Classify the preparation.
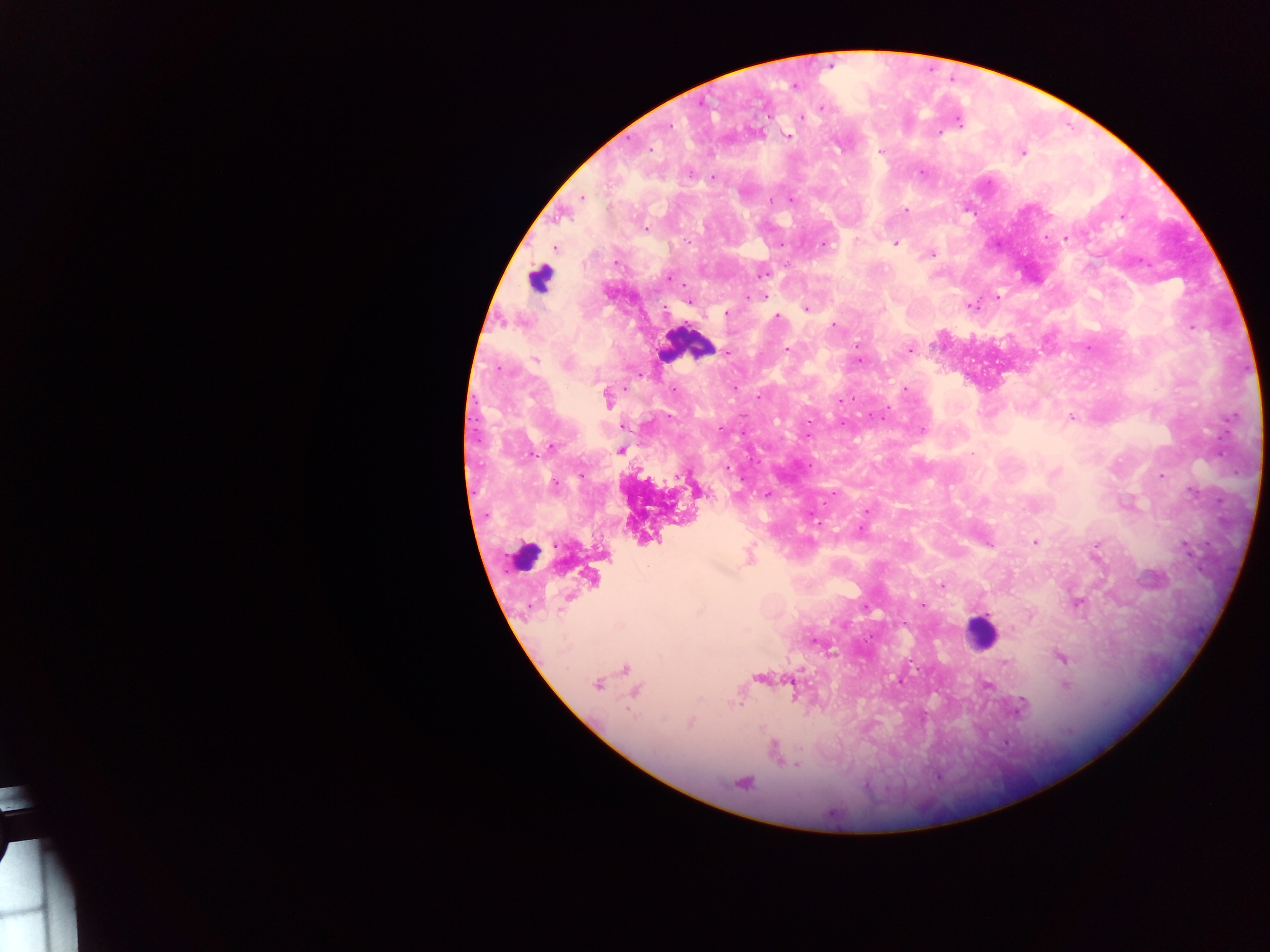
Thick blood film.

Approximate centers as {x, y} in pixels. Leukocyte locations: {540, 277}, {686, 344}, {522, 556}, {980, 631}. Plasmodium parasite locations: {829, 66}, {794, 85}, {823, 107}, {801, 117}, {959, 123}, {668, 125}, {939, 132}, {786, 136}, {649, 149}, {881, 152}, {1021, 152}, {921, 172}, {712, 177}, {582, 197}, {905, 211}, {1122, 217}, {646, 228}, {1066, 238}, {824, 243}, {895, 243}, {553, 247}, {930, 253}, {762, 272}, {671, 278}, {764, 296}, {997, 297}, {688, 300}, {971, 306}, {806, 308}, {726, 313}, {778, 317}, {833, 325}, {1192, 327}, {787, 349}, {909, 349}, {727, 352}, {535, 359}, {858, 360}, {672, 390}, {904, 390}, {606, 397}, {1070, 417}, {624, 425}, {922, 430}, {551, 447}, {620, 450}, {726, 469}, {1162, 476}, {554, 484}, {698, 489}, {766, 494}, {866, 511}, {1035, 542}, {987, 543}, {1095, 550}, {748, 556}, {591, 577}, {941, 585}, {1077, 603}, {923, 605}, {816, 642}, {1061, 657}, {625, 668}, {759, 677}, {791, 679}, {597, 683}, {986, 685}, {1066, 685}, {635, 692}, {774, 751}, {798, 765}, {742, 782}. Image is 1270×952 pixels. Mobile-phone photograph taken through the microscope. Single field of view. Sample from Ghana.